Describe the morphology of the erythrocytes.
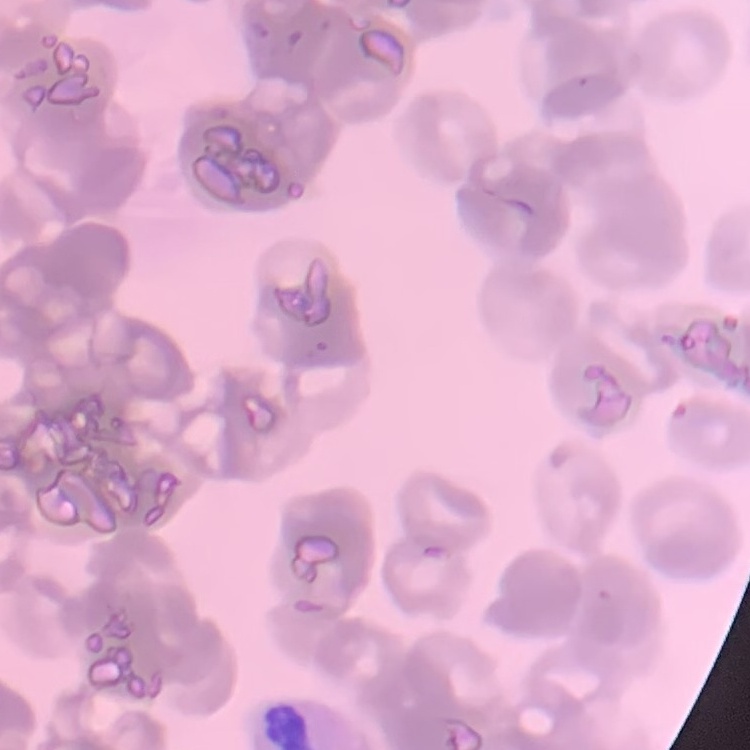
They show rouleaux formation.

{
  "stain": "Field's or Giemsa",
  "image_type": "square crop of a larger photomicrograph",
  "preparation": "thin blood film"
}